Report the malaria status of this cell.
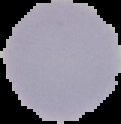
Uninfected.

From a thin blood film. Cell region segmented out of the field of view; the surrounding area is masked to black. Image is 121×124 pixels.